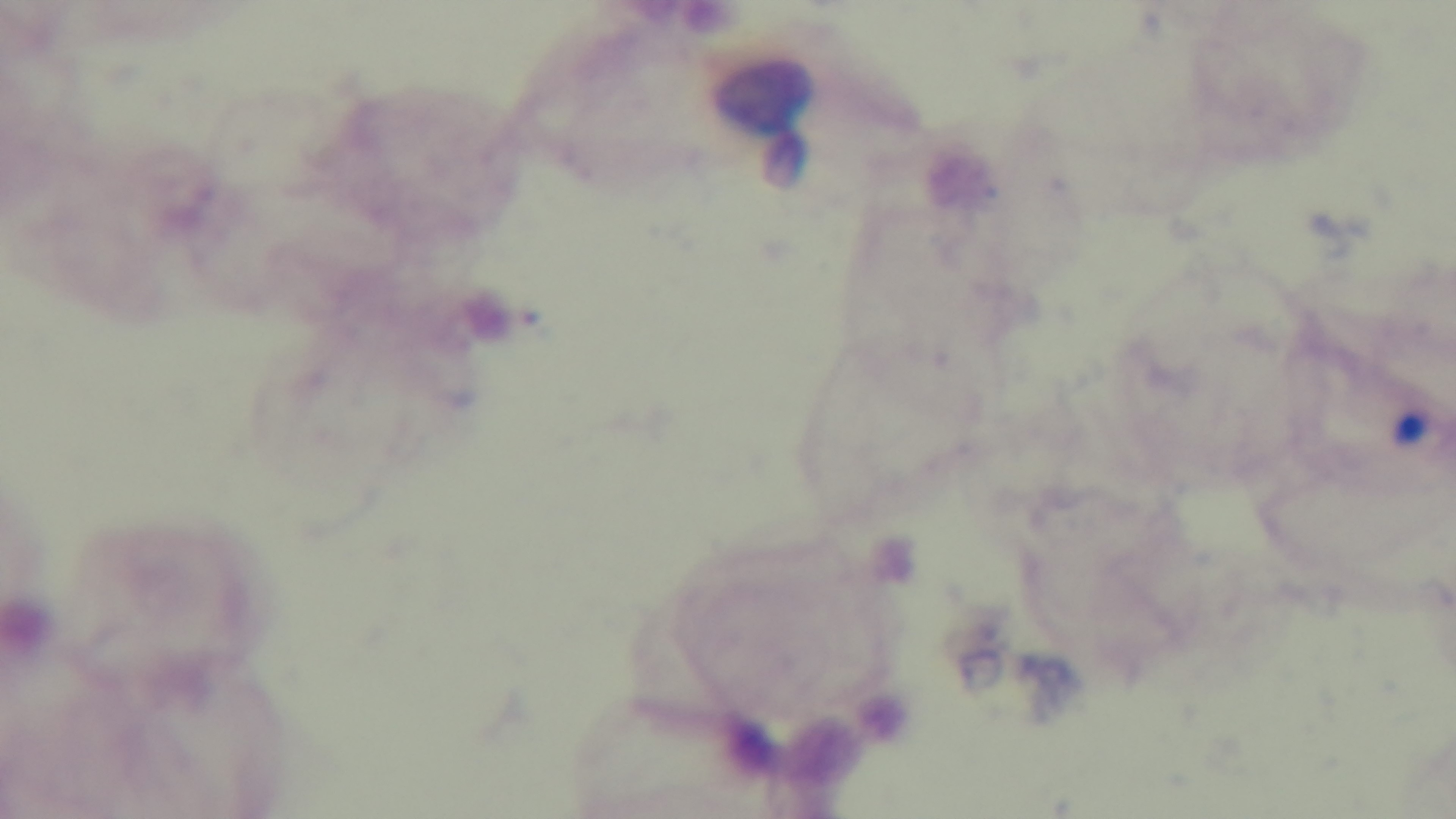

Preparation: thick smear. One field from the slide. Oil-immersion objective, 100x. Light microscopy. Giemsa-stained. Malaria status: uninfected. Captured with a mounted 4K digital camera.